Classify this cell by malaria status.
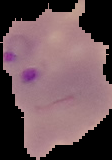
It is parasitized.

Image is 112×160 pixels. The area outside the segmented cell region is set to black. From a thin blood smear.